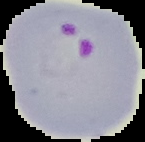

Summary:
  - Result: malaria parasites identified
  - Image type: cell region segmented out of the field of view; surrounding area masked to black
  - Image size: 145×142 pixels
  - Preparation: thin blood smear